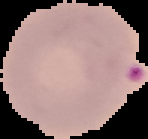
Summary:
  - Preparation: thin blood smear
  - Image type: segmented cell region with the area outside set to black
  - Malaria status: parasitized
  - Image size: 148×139 pixels